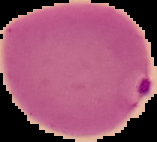
Image is 157×142 pixels. Result: Plasmodium parasites identified. Segmented cell region on a black background. From a thin blood smear.